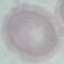
result: no malaria parasites seen
preparation: thin blood smear
stain: Giemsa
capture: smartphone through the microscope eyepiece
image_type: automatically extracted cell patch, resized to 64 × 64 pixels